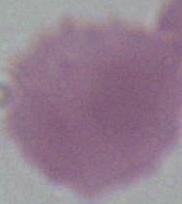
An erythrocyte is seen. Captured at 1000x magnification. Photomicrograph.